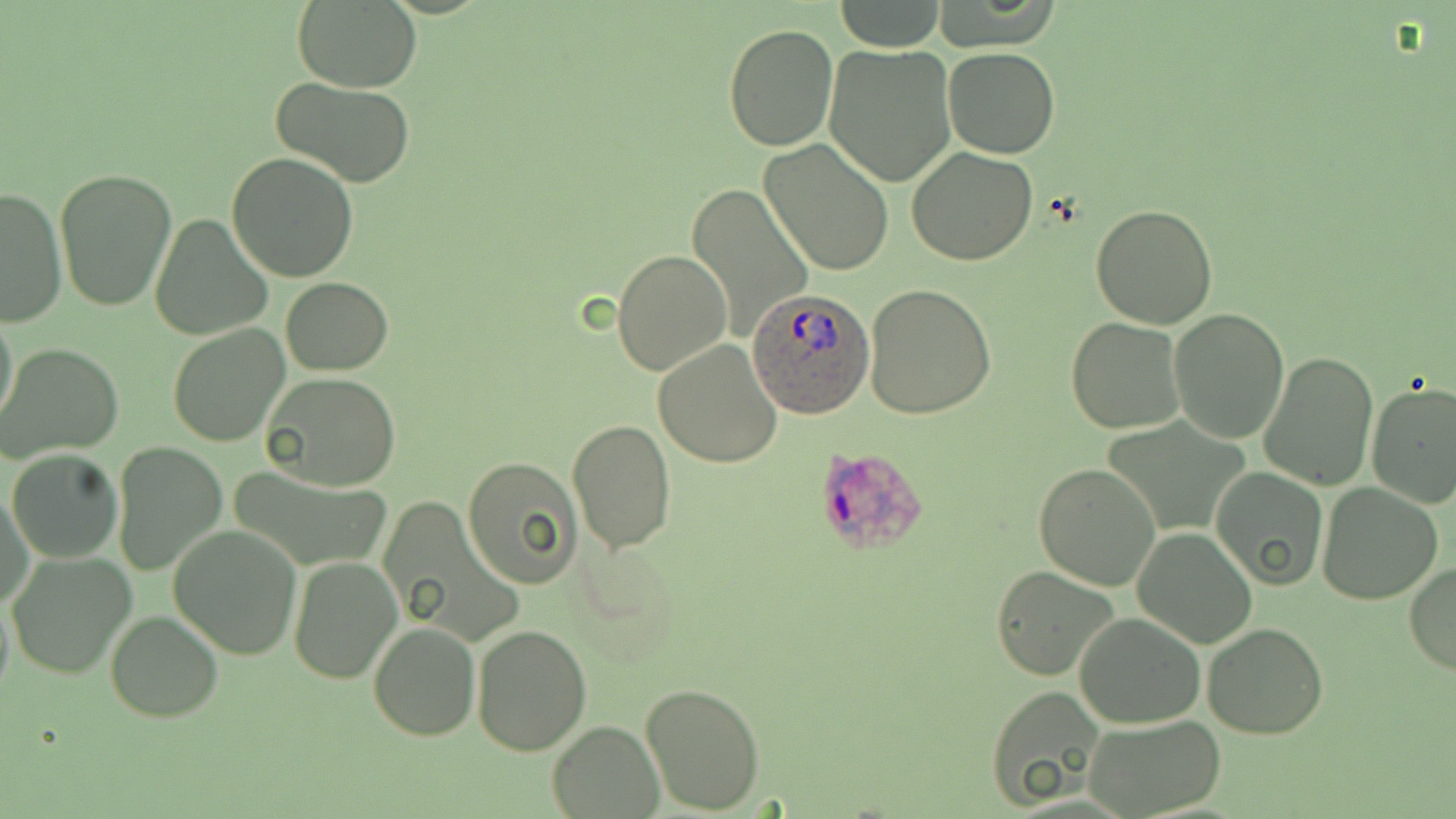 Approximate bounding boxes as named x1/y1/x2/y2 corners in pixels. Uninfected red blood cell locations: (x1=291, y1=0, x2=422, y2=93), (x1=834, y1=1, x2=945, y2=52), (x1=721, y1=22, x2=838, y2=152), (x1=823, y1=43, x2=957, y2=187), (x1=944, y1=47, x2=1059, y2=159), (x1=272, y1=77, x2=417, y2=188), (x1=759, y1=138, x2=894, y2=277), (x1=906, y1=146, x2=1038, y2=265), (x1=227, y1=154, x2=360, y2=282), (x1=55, y1=167, x2=178, y2=312), (x1=687, y1=184, x2=814, y2=342), (x1=1, y1=186, x2=67, y2=327), (x1=1091, y1=205, x2=1218, y2=330), (x1=150, y1=215, x2=271, y2=340), (x1=611, y1=249, x2=732, y2=376), (x1=281, y1=277, x2=392, y2=374), (x1=865, y1=283, x2=998, y2=418), (x1=1, y1=309, x2=19, y2=434), (x1=1168, y1=309, x2=1290, y2=442), (x1=1065, y1=318, x2=1185, y2=436), (x1=167, y1=323, x2=291, y2=446), (x1=653, y1=340, x2=784, y2=468), (x1=2, y1=342, x2=124, y2=462), (x1=1259, y1=351, x2=1380, y2=491), (x1=260, y1=372, x2=402, y2=491), (x1=1365, y1=382, x2=1456, y2=507), (x1=568, y1=419, x2=676, y2=555), (x1=113, y1=442, x2=227, y2=576), (x1=7, y1=449, x2=124, y2=562), (x1=463, y1=457, x2=583, y2=587), (x1=1033, y1=464, x2=1162, y2=591), (x1=1211, y1=468, x2=1328, y2=590), (x1=1, y1=483, x2=33, y2=612), (x1=1316, y1=483, x2=1442, y2=604), (x1=169, y1=524, x2=302, y2=661), (x1=1132, y1=527, x2=1257, y2=649), (x1=6, y1=550, x2=137, y2=680), (x1=289, y1=556, x2=401, y2=682), (x1=1406, y1=561, x2=1456, y2=675), (x1=990, y1=565, x2=1122, y2=681), (x1=0, y1=588, x2=14, y2=705), (x1=105, y1=611, x2=224, y2=722), (x1=1074, y1=612, x2=1205, y2=730), (x1=367, y1=619, x2=480, y2=740), (x1=1202, y1=620, x2=1329, y2=738), (x1=471, y1=624, x2=594, y2=755), (x1=639, y1=682, x2=766, y2=813), (x1=983, y1=688, x2=1107, y2=810), (x1=1080, y1=714, x2=1226, y2=817), (x1=548, y1=721, x2=664, y2=817). Plasmodium ovale-infected red blood cell locations: (x1=747, y1=290, x2=873, y2=418), (x1=811, y1=443, x2=928, y2=557). Slide-level diagnosis: Plasmodium ovale. Image is 1456×819 pixels. May-Grünwald-Giemsa-stained preparation. 1000x magnification. Light microscopy. Single field of view. Thin blood film.